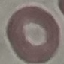

Summary:
  - Malaria status: uninfected
  - Stain: Giemsa
  - Capture: smartphone through the microscope eyepiece
  - Preparation: thin blood smear
  - Image type: cell patch, automatically extracted from a larger field of view and resized to 64 × 64 pixels